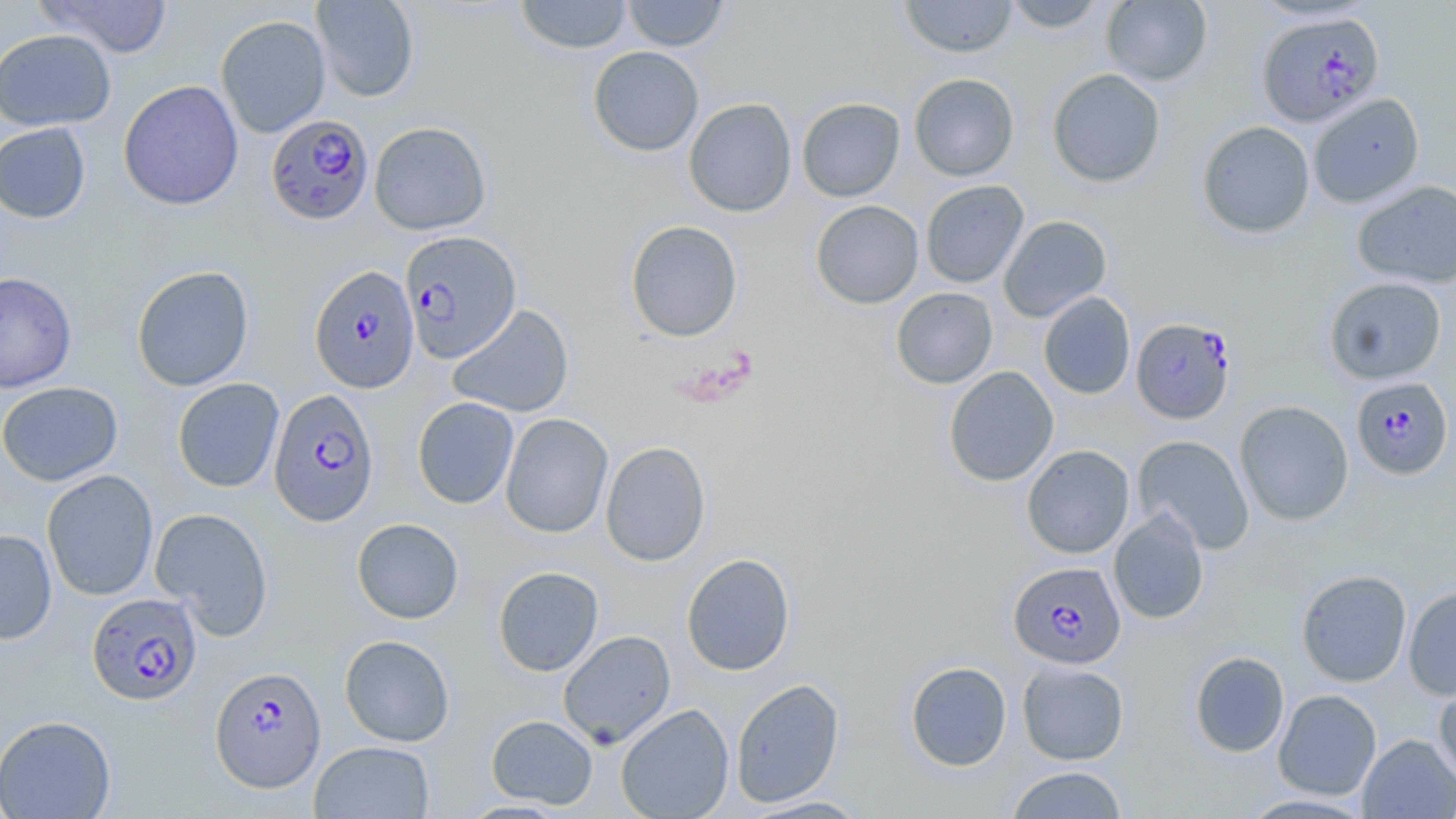

slide-level diagnosis = Plasmodium falciparum
modality = light microscopy
stain = May-Grünwald-Giemsa
image size = 1456×819 pixels
preparation = thin blood film
field of view = one of a larger specimen
uninfected red blood cell locations = approximate bounding boxes as named x1/y1/x2/y2 corners in pixels: (x1=35, y1=0, x2=174, y2=58), (x1=312, y1=0, x2=419, y2=102), (x1=515, y1=0, x2=632, y2=53), (x1=622, y1=0, x2=729, y2=52), (x1=900, y1=0, x2=1017, y2=58), (x1=1002, y1=0, x2=1107, y2=33), (x1=1101, y1=0, x2=1213, y2=87), (x1=216, y1=15, x2=331, y2=138), (x1=0, y1=29, x2=115, y2=131), (x1=588, y1=46, x2=704, y2=156), (x1=1047, y1=68, x2=1166, y2=188), (x1=909, y1=73, x2=1020, y2=181), (x1=118, y1=80, x2=244, y2=210), (x1=1308, y1=93, x2=1425, y2=208), (x1=797, y1=97, x2=905, y2=202), (x1=683, y1=98, x2=797, y2=217), (x1=1197, y1=120, x2=1315, y2=238), (x1=369, y1=121, x2=491, y2=235), (x1=0, y1=123, x2=91, y2=223), (x1=920, y1=180, x2=1029, y2=288), (x1=1352, y1=180, x2=1456, y2=289), (x1=811, y1=200, x2=924, y2=309), (x1=998, y1=215, x2=1112, y2=323), (x1=625, y1=220, x2=743, y2=342), (x1=131, y1=265, x2=254, y2=391), (x1=0, y1=271, x2=77, y2=393), (x1=1324, y1=276, x2=1447, y2=384), (x1=891, y1=287, x2=999, y2=389), (x1=1038, y1=292, x2=1136, y2=399), (x1=447, y1=304, x2=574, y2=418), (x1=943, y1=366, x2=1059, y2=487), (x1=172, y1=377, x2=285, y2=492), (x1=0, y1=381, x2=123, y2=486), (x1=412, y1=396, x2=519, y2=509), (x1=1234, y1=400, x2=1354, y2=526), (x1=500, y1=413, x2=613, y2=538), (x1=1132, y1=435, x2=1255, y2=555), (x1=600, y1=440, x2=712, y2=566), (x1=1021, y1=444, x2=1135, y2=559), (x1=42, y1=469, x2=159, y2=601), (x1=150, y1=507, x2=274, y2=640), (x1=1108, y1=508, x2=1210, y2=625), (x1=351, y1=518, x2=464, y2=624), (x1=0, y1=529, x2=58, y2=645), (x1=681, y1=553, x2=796, y2=676), (x1=493, y1=566, x2=604, y2=676), (x1=1296, y1=569, x2=1412, y2=687), (x1=1403, y1=586, x2=1456, y2=700), (x1=558, y1=630, x2=676, y2=748), (x1=339, y1=634, x2=455, y2=746), (x1=1190, y1=651, x2=1290, y2=758), (x1=905, y1=661, x2=1012, y2=771), (x1=1017, y1=661, x2=1129, y2=765), (x1=730, y1=678, x2=845, y2=808), (x1=1433, y1=681, x2=1456, y2=788), (x1=1273, y1=689, x2=1381, y2=800), (x1=615, y1=703, x2=734, y2=819), (x1=0, y1=714, x2=116, y2=819), (x1=486, y1=714, x2=598, y2=809), (x1=1358, y1=734, x2=1456, y2=818), (x1=309, y1=740, x2=435, y2=818), (x1=1005, y1=765, x2=1129, y2=818), (x1=1236, y1=793, x2=1377, y2=818), (x1=740, y1=795, x2=873, y2=818)
magnification = 1000x
Plasmodium falciparum-infected red blood cell locations = approximate bounding boxes as named x1/y1/x2/y2 corners in pixels: (x1=1256, y1=11, x2=1385, y2=128), (x1=266, y1=114, x2=375, y2=226), (x1=399, y1=230, x2=522, y2=364), (x1=310, y1=266, x2=420, y2=392), (x1=1131, y1=317, x2=1236, y2=423), (x1=1350, y1=376, x2=1454, y2=479), (x1=268, y1=388, x2=379, y2=525), (x1=1009, y1=561, x2=1126, y2=670), (x1=87, y1=592, x2=203, y2=706), (x1=210, y1=665, x2=326, y2=793)